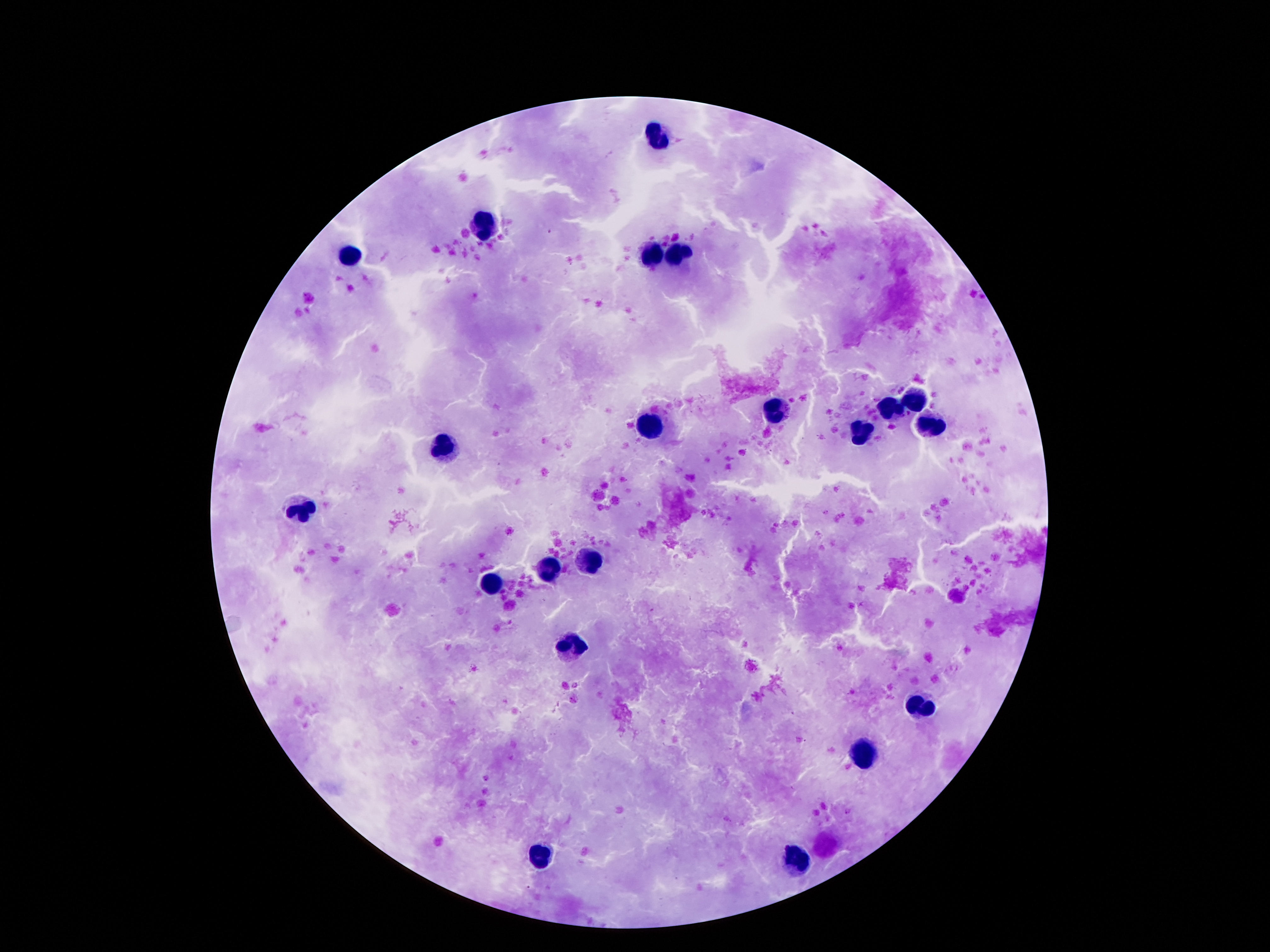
Approximate centers as [x, y] in pixels.
Summary:
  - Leukocyte locations: [656, 135], [480, 225], [350, 252], [684, 255], [652, 258], [916, 399], [889, 408], [779, 410], [650, 425], [932, 428], [861, 430], [445, 444], [303, 512], [592, 558], [547, 569], [492, 583], [568, 649], [920, 707], [861, 750], [539, 855], [795, 858]
  - Patient malaria status: uninfected
  - Stain: Giemsa
  - Capture: smartphone camera through the microscope eyepiece
  - Image size: 1270×952 pixels
  - Preparation: thick blood film
  - Field of view: one from this slide
  - Magnification: 100x